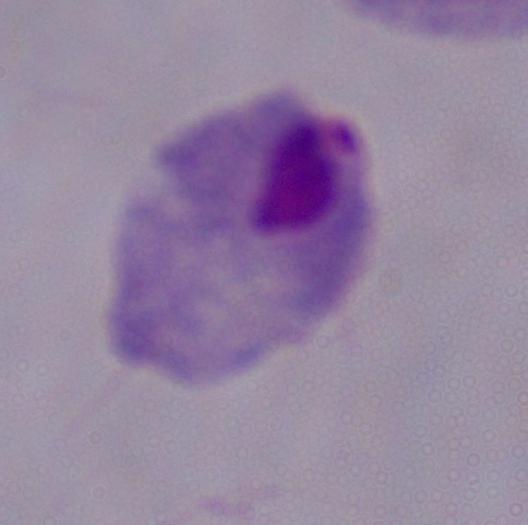 A trichomonad is seen. Captured at 1000x magnification. Micrograph.